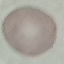

Summary:
  - Malaria status: uninfected
  - Capture: smartphone camera at the microscope eyepiece
  - Stain: Giemsa
  - Image type: automatically extracted cell patch, resized to 64 × 64 pixels
  - Preparation: thin smear